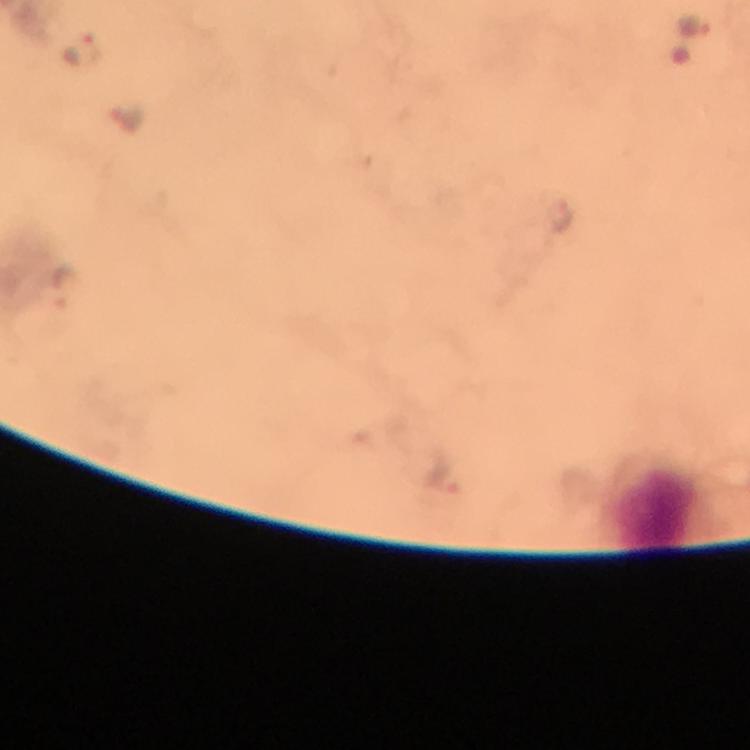

context: from a malaria diagnostic workup
immersion_oil: applied
cropped_from: one field of view
stain: Giemsa
leukocyte_locations: 'approximate centers as [x, y] in pixels: [653, 510]'
capture: smartphone camera through the microscope
preparation: thick blood smear
plasmodium_parasite_locations: 'approximate centers as [x, y] in pixels: [692, 24], [79, 49], [561, 220], [61, 286], [445, 473]'
magnification: 100x
image_size: 750×750 pixels